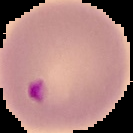
Summary:
  - Malaria status: parasitized
  - Image size: 133×133 pixels
  - Image type: segmented cell region on a black background
  - Preparation: thin blood smear